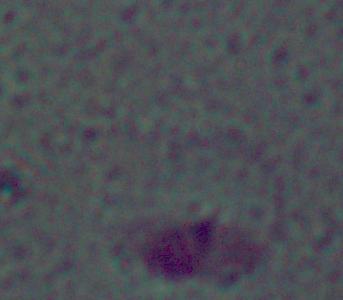

modality: micrograph
identification: Leishmania
magnification: 1000x